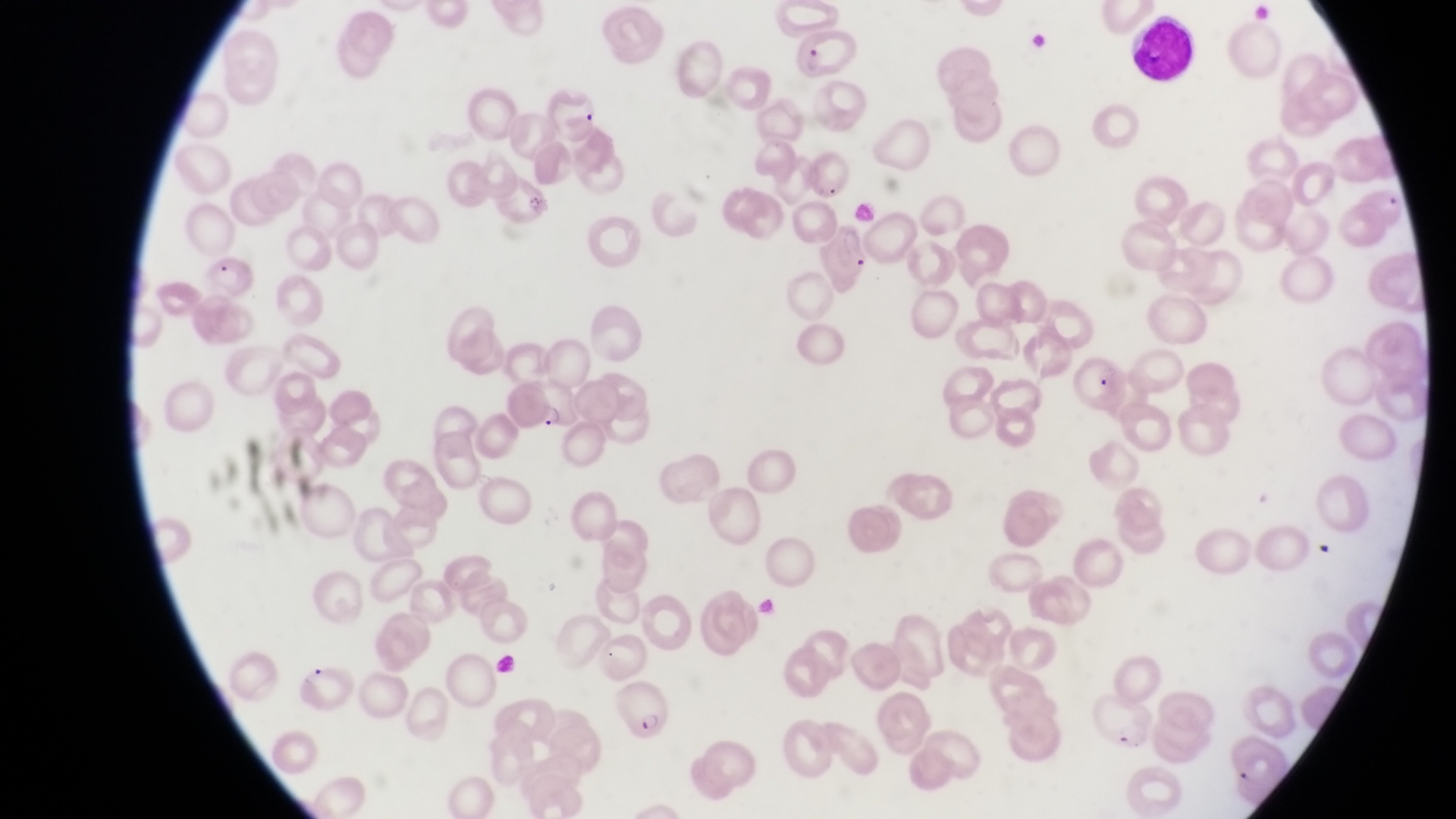 Approximate bounding boxes as left top right bottom in pixels. Leukocyte locations: 1131 14 1200 85. Parasitised red blood cell locations: 798 36 861 81; 821 228 873 288; 208 257 258 303; 1075 353 1125 414; 522 377 580 432; 298 658 356 715; 614 679 673 745; 1096 695 1151 754. Photographed through the eyepiece of an Olympus CX-23 microscope with a smartphone camera. Image is 1456×819 pixels. Thin blood film. Sample from Uganda. At a magnification of 1000x. Single field of view.